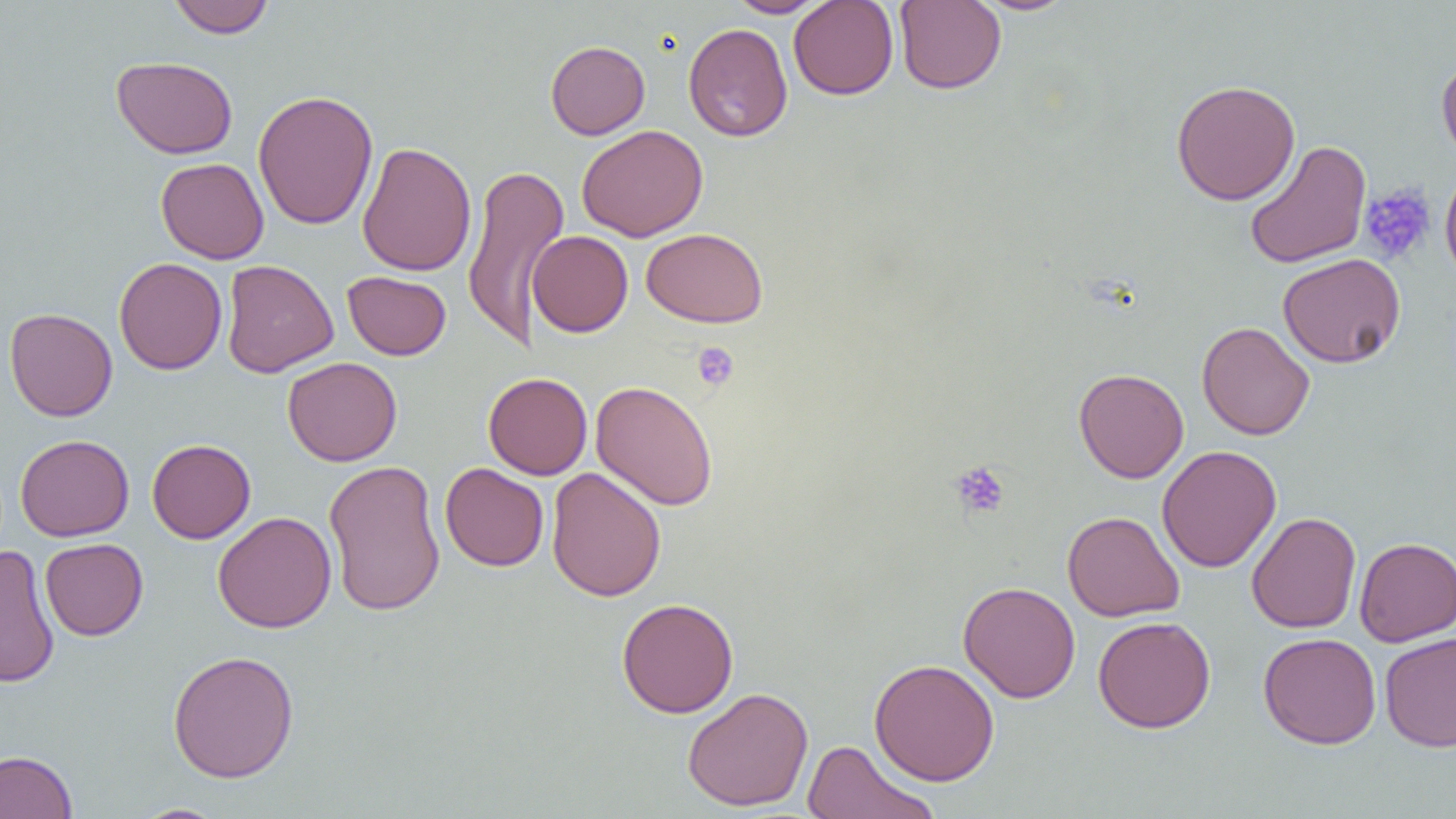

{
  "slide_level_diagnosis": "no evidence of blood parasites",
  "platelet_locations": "approximate bounding boxes as [x1, y1, x2, y2] in pixels: [1360, 184, 1436, 264], [693, 341, 739, 390], [950, 460, 1011, 519]",
  "image_size": "1456×819 pixels",
  "preparation": "thin blood film",
  "uninfected_red_blood_cell_locations": "approximate bounding boxes as [x1, y1, x2, y2] in pixels: [167, 0, 275, 38], [726, 0, 830, 18], [788, 0, 899, 100], [894, 0, 1006, 94], [972, 0, 1079, 15], [683, 23, 793, 141], [545, 40, 650, 139], [1436, 53, 1456, 166], [111, 56, 238, 159], [1171, 79, 1300, 205], [252, 89, 379, 230], [577, 124, 708, 242], [1244, 139, 1371, 269], [357, 141, 476, 277], [155, 158, 269, 264], [462, 162, 570, 350], [1439, 165, 1456, 287], [641, 227, 768, 328], [528, 230, 633, 337], [1278, 253, 1406, 368], [114, 257, 227, 375], [221, 259, 338, 377], [342, 271, 451, 360], [4, 307, 118, 422], [1196, 321, 1315, 440], [282, 357, 402, 466], [1074, 368, 1189, 483], [483, 372, 592, 479], [590, 380, 719, 511], [15, 434, 134, 541], [147, 439, 256, 543], [1157, 445, 1281, 573], [323, 459, 446, 617], [440, 463, 549, 571], [546, 467, 666, 602], [213, 511, 337, 633], [1062, 511, 1185, 622], [1246, 511, 1361, 634], [1354, 536, 1456, 646], [40, 538, 148, 640], [0, 545, 60, 689], [958, 581, 1081, 703], [616, 597, 739, 718], [1093, 615, 1216, 733], [1379, 631, 1456, 752], [1258, 632, 1382, 749], [167, 650, 300, 783], [869, 658, 1000, 786], [682, 687, 814, 812], [799, 739, 941, 819], [0, 749, 78, 819], [130, 803, 230, 819]",
  "magnification": "1000x",
  "modality": "optical microscopy",
  "field_of_view": "single"
}